State which parasite is depicted.
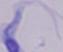
This is a trypanosome.

modality: photomicrograph
magnification: 1000x